Locate every Plasmodium parasite.
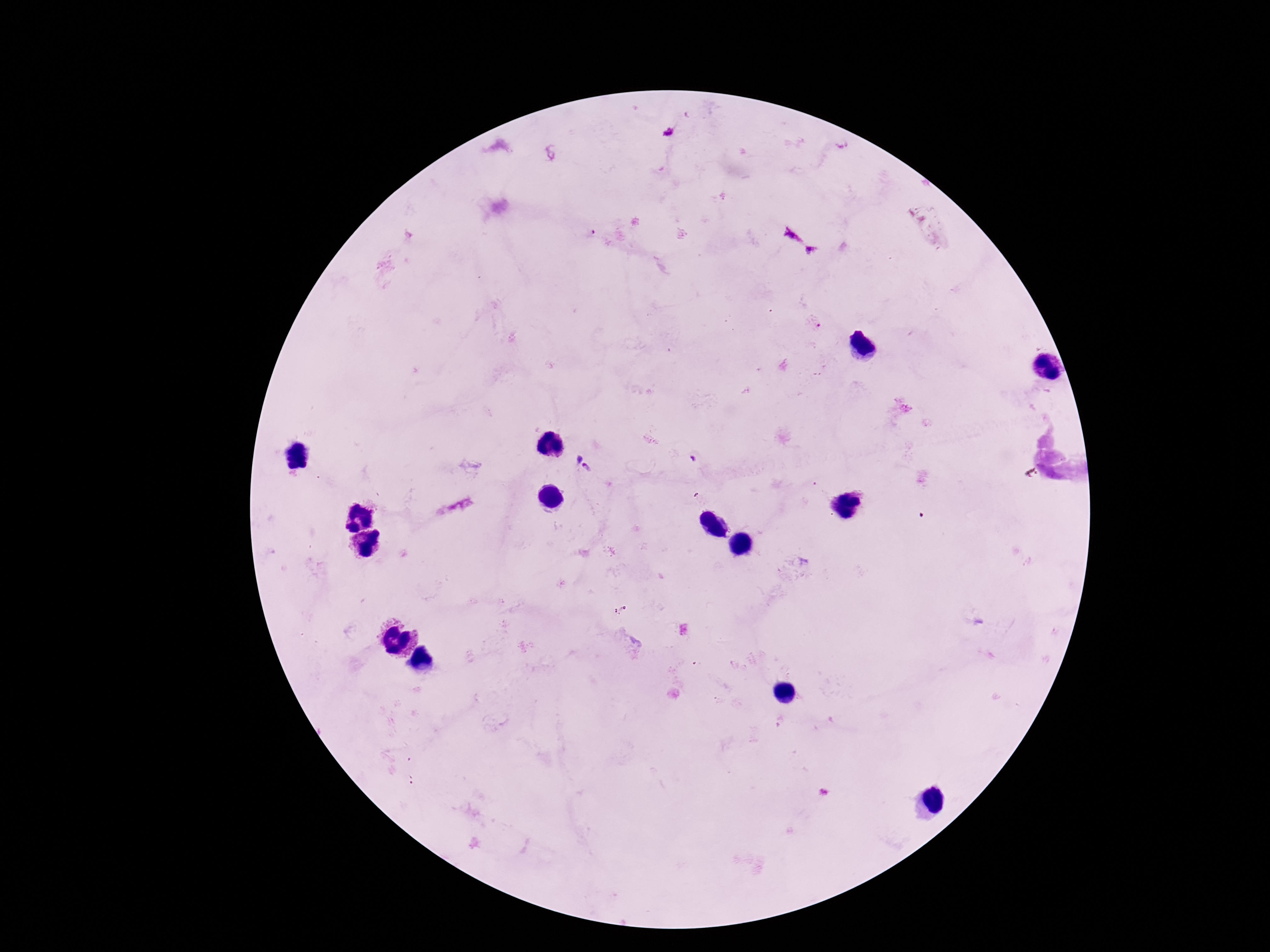

Approximate centers as {x, y} in pixels.
Plasmodium parasites: {668, 131}, {792, 235}, {811, 250}, {579, 458}, {586, 468}.

field of view = single
capture = smartphone camera through the microscope eyepiece
preparation = thick peripheral-blood smear
magnification = 100x
patient malaria status = infected
image size = 1270×952 pixels
stain = Giemsa